Give the extent of all Trypanosoma brucei.
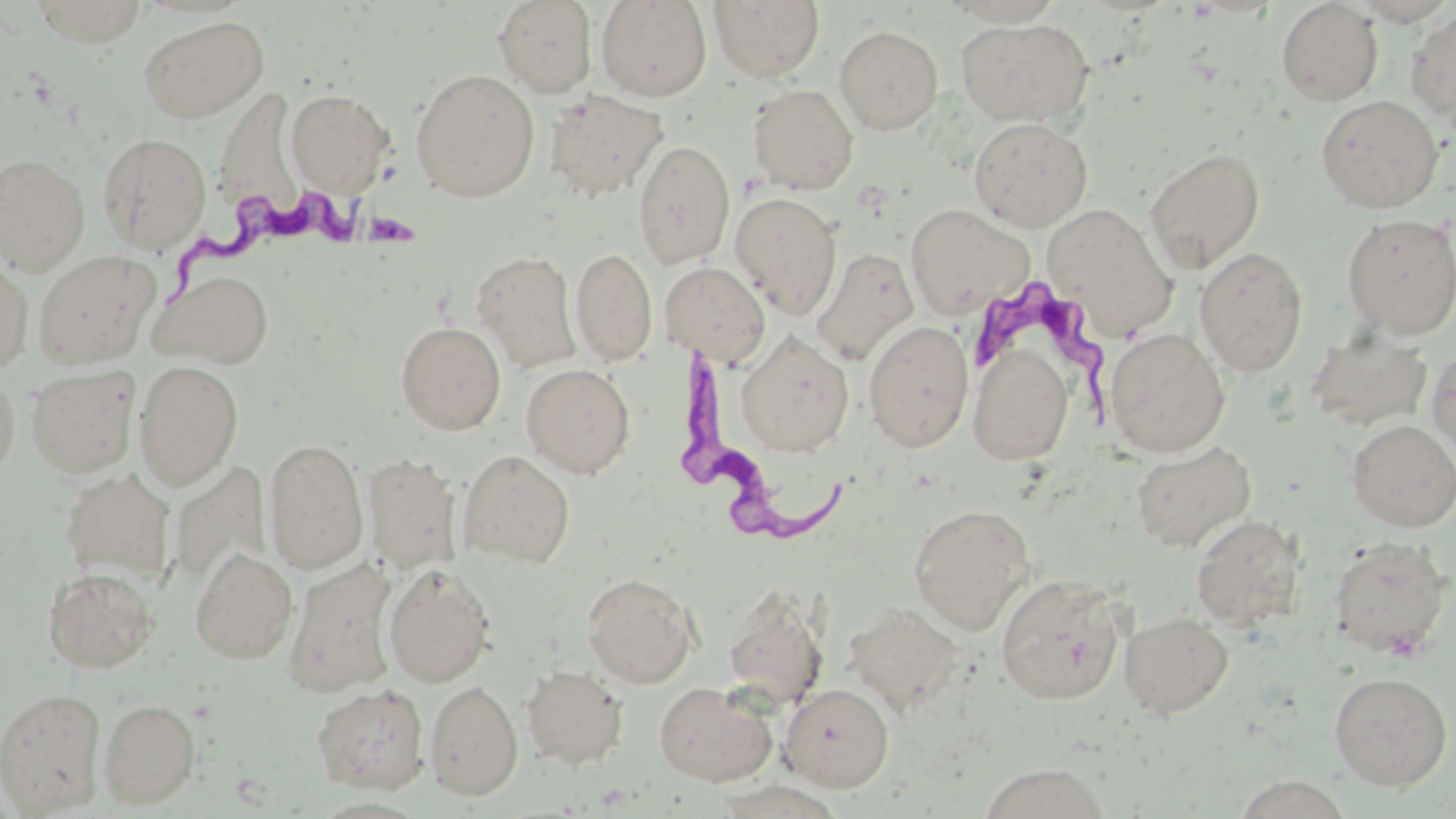

Approximate bounding boxes as [x1, y1, x2, y2] in pixels.
Trypanosoma brucei: [169, 184, 412, 313], [971, 279, 1131, 438], [665, 348, 846, 558].

Uninfected red blood cell locations: [29, 0, 149, 46], [493, 0, 597, 97], [596, 0, 712, 101], [709, 1, 825, 83], [1276, 1, 1383, 106], [1406, 9, 1456, 127], [138, 15, 268, 123], [955, 17, 1093, 126], [835, 25, 944, 134], [410, 68, 540, 201], [748, 84, 859, 194], [214, 88, 301, 213], [285, 89, 394, 194], [544, 90, 667, 202], [1316, 94, 1443, 213], [968, 117, 1093, 231], [96, 132, 212, 254], [633, 140, 735, 269], [0, 145, 202, 270], [1145, 146, 1265, 271], [0, 153, 90, 274], [730, 192, 843, 319], [1042, 203, 1177, 339], [904, 204, 1034, 319], [1340, 213, 1456, 339], [1194, 246, 1308, 377], [571, 247, 656, 366], [810, 248, 918, 365], [33, 250, 161, 370], [472, 251, 581, 372], [0, 254, 33, 375], [659, 261, 770, 364], [150, 270, 274, 368], [396, 321, 506, 434], [863, 321, 974, 452], [1105, 330, 1230, 457], [1306, 332, 1433, 431], [737, 333, 855, 455], [967, 344, 1074, 465], [1427, 346, 1456, 461], [133, 360, 244, 491], [521, 363, 635, 478], [25, 365, 140, 478], [0, 368, 20, 492], [1347, 420, 1456, 531], [263, 438, 368, 574], [1130, 442, 1256, 553], [457, 449, 575, 568], [363, 452, 462, 576], [59, 469, 175, 585], [908, 503, 1035, 634], [1191, 515, 1304, 628], [1329, 536, 1453, 660], [190, 547, 297, 664], [283, 559, 398, 699], [383, 563, 496, 687], [42, 565, 159, 674], [582, 572, 700, 687], [995, 575, 1126, 705], [722, 584, 828, 709], [842, 603, 963, 716], [1119, 612, 1233, 719], [521, 665, 628, 769], [1329, 671, 1453, 791], [425, 681, 523, 800], [654, 681, 777, 786], [311, 683, 430, 794], [779, 683, 894, 791], [1, 686, 107, 816], [99, 698, 201, 808], [978, 763, 1109, 818], [712, 780, 846, 818]. Slide-level diagnosis: Trypanosoma brucei. 1000x magnification. May-Grünwald-Giemsa-stained preparation. Thin blood smear. Image is 1456×819 pixels. Light microscopy. Single field of view.